Assess this cell for malaria.
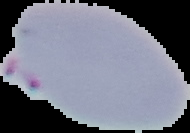

It is parasitized.

Summary:
  - Preparation: thin blood film
  - Image size: 190×133 pixels
  - Image type: segmented cell region with the area outside set to black